Assess this cell for malaria.
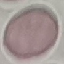

Uninfected.

Thin blood film. Cell patch, automatically extracted from a larger field of view and resized to 64 × 64 pixels. Photographed with a smartphone camera at the microscope eyepiece. Giemsa-stained preparation.